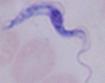
A trypanosome is shown. Micrograph. Captured at 1000x magnification.